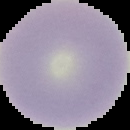

image type = segmented cell region on a black background
malaria status = uninfected
image size = 130×130 pixels
preparation = thin blood smear